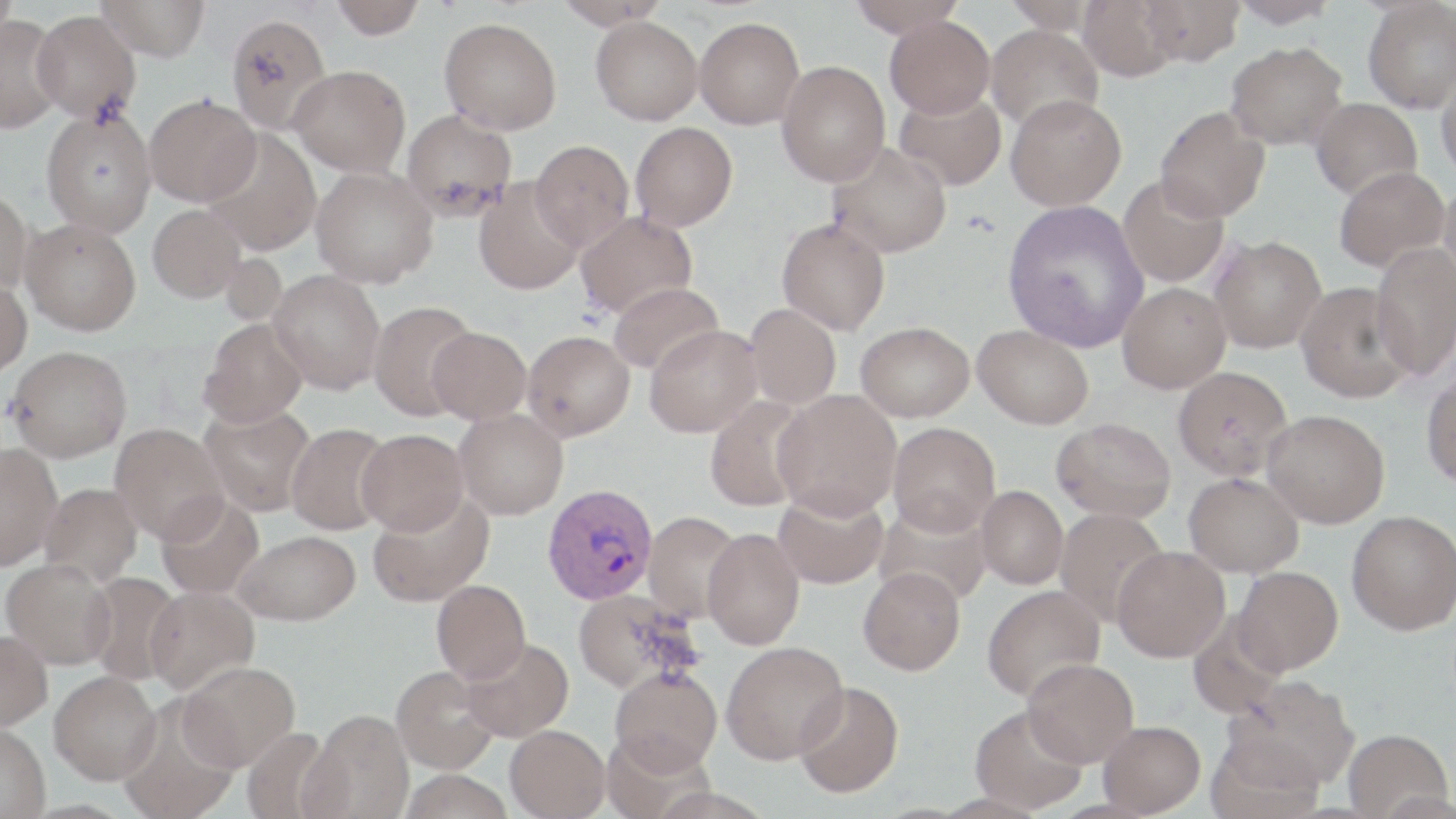

slide-level diagnosis = Plasmodium vivax
image size = 1456×819 pixels
field of view = single
modality = light microscopy
Plasmodium vivax-infected red blood cell locations = approximate bounding boxes as [x1, y1, x2, y2] in pixels: [543, 483, 658, 604]
magnification = 1000x
preparation = thin blood smear
uninfected red blood cell locations = approximate bounding boxes as [x1, y1, x2, y2] in pixels: [0, 0, 18, 50], [96, 0, 210, 62], [552, 0, 672, 29], [849, 0, 965, 36], [1003, 0, 1100, 34], [1079, 0, 1183, 81], [1139, 0, 1245, 66], [1228, 0, 1339, 28], [1362, 0, 1456, 113], [330, 1, 426, 39], [31, 10, 141, 124], [224, 12, 332, 136], [0, 15, 65, 133], [886, 15, 995, 119], [591, 16, 702, 125], [694, 16, 805, 129], [439, 17, 562, 134], [985, 23, 1104, 131], [1225, 41, 1348, 150], [776, 61, 890, 187], [290, 65, 410, 176], [1436, 69, 1456, 180], [894, 88, 1007, 191], [144, 94, 261, 206], [1005, 94, 1127, 211], [1310, 98, 1422, 200], [1155, 106, 1270, 222], [40, 107, 157, 236], [401, 109, 517, 221], [630, 122, 738, 232], [202, 129, 321, 256], [529, 141, 634, 250], [827, 141, 952, 258], [311, 166, 438, 288], [1333, 166, 1449, 272], [1118, 174, 1230, 287], [474, 177, 585, 295], [1438, 182, 1456, 298], [0, 189, 33, 297], [1002, 199, 1150, 352], [148, 204, 246, 303], [574, 211, 698, 319], [777, 217, 890, 335], [20, 218, 141, 335], [1209, 235, 1327, 353], [1370, 242, 1456, 380], [268, 269, 386, 394], [0, 276, 32, 377], [608, 281, 724, 375], [1296, 281, 1416, 403], [1117, 282, 1231, 393], [368, 300, 478, 420], [745, 303, 842, 410], [200, 318, 307, 428], [856, 321, 975, 422], [644, 324, 763, 437], [973, 324, 1094, 429], [427, 327, 531, 424], [523, 330, 635, 441], [7, 345, 132, 461], [1173, 366, 1293, 481], [1421, 370, 1456, 488], [772, 390, 902, 519], [704, 395, 813, 512], [200, 404, 316, 516], [454, 409, 568, 520], [1262, 409, 1390, 528], [1053, 417, 1175, 522], [888, 421, 1000, 536], [286, 422, 393, 535], [109, 423, 229, 544], [356, 428, 469, 535], [0, 442, 62, 570], [1184, 472, 1303, 577], [39, 482, 142, 586], [976, 486, 1068, 589], [368, 490, 494, 606], [773, 490, 888, 589], [156, 494, 264, 599], [874, 502, 992, 607], [1054, 507, 1168, 625], [1347, 510, 1456, 635], [643, 512, 744, 623], [703, 527, 805, 649], [235, 529, 361, 626], [1112, 546, 1230, 662], [1, 559, 116, 670], [1233, 566, 1343, 675], [858, 567, 966, 675], [83, 571, 185, 686], [432, 580, 531, 683], [982, 584, 1105, 702], [144, 586, 258, 694], [572, 588, 700, 693], [0, 631, 53, 734], [461, 637, 574, 742], [721, 641, 849, 764], [1022, 657, 1139, 768], [176, 660, 300, 772], [392, 665, 498, 774], [609, 666, 722, 775], [49, 673, 161, 788], [1226, 674, 1359, 791], [793, 681, 904, 798], [118, 701, 240, 819], [970, 705, 1088, 814], [303, 710, 415, 818], [1098, 720, 1205, 816], [505, 724, 610, 818], [241, 726, 336, 819], [0, 727, 50, 819], [1342, 729, 1452, 819], [1206, 734, 1325, 819], [399, 769, 513, 819], [21, 800, 140, 819]
stain = May-Grünwald-Giemsa